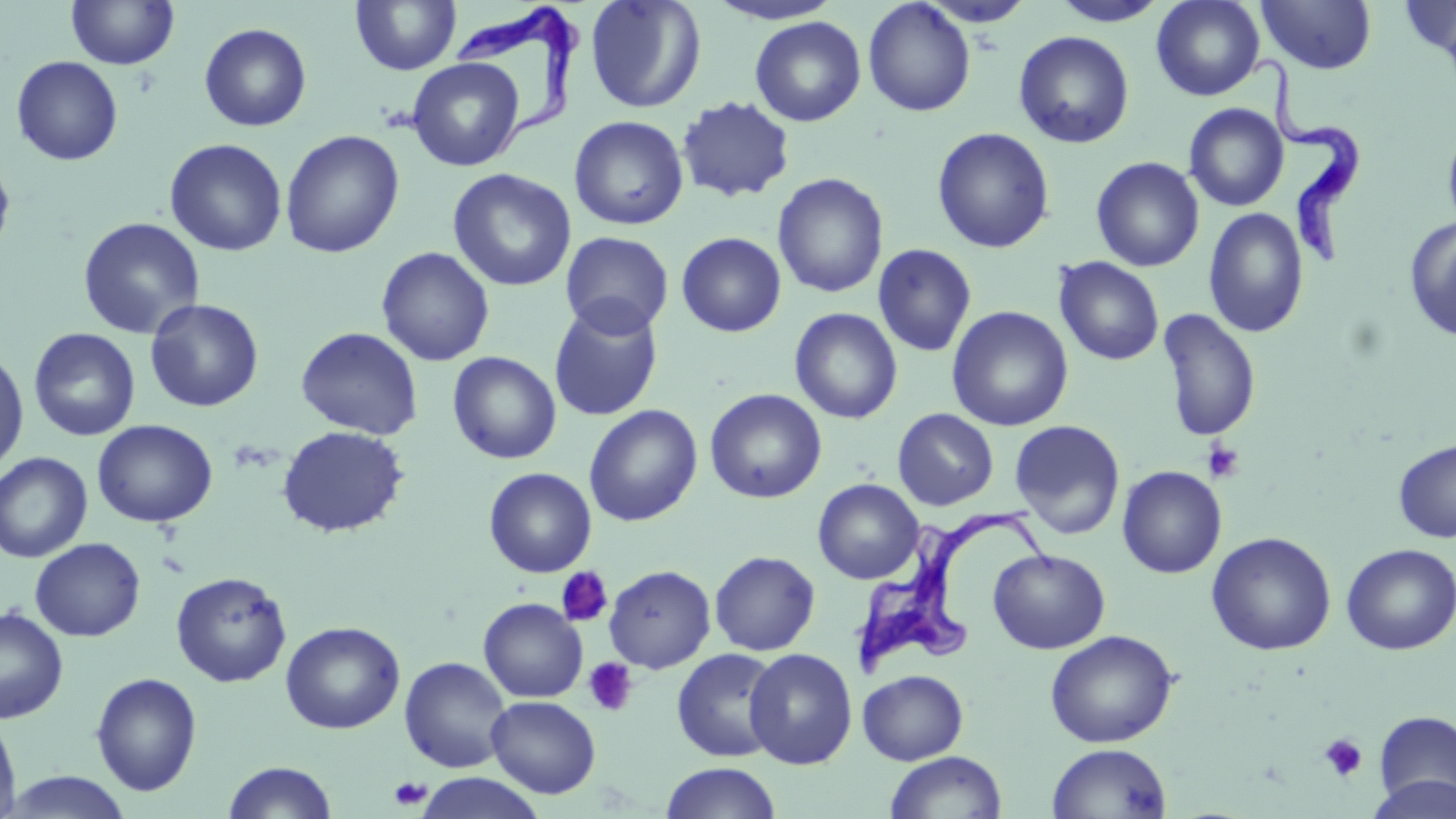 Approximate bounding boxes as (x1,y1)-(x2,y2) corner pairs in pixels. Platelet locations: (1201,439)-(1245,483), (555,568)-(612,627), (584,657)-(638,716), (1319,733)-(1367,782), (388,776)-(432,809). Trypanosoma brucei locations: (451,10)-(586,169), (1253,56)-(1363,274), (851,507)-(1061,685). Uninfected red blood cell locations: (66,0)-(179,69), (350,0)-(462,76), (584,0)-(706,114), (705,0)-(844,26), (1051,0)-(1170,27), (1151,0)-(1265,101), (1256,0)-(1377,75), (1398,0)-(1456,68), (863,1)-(976,117), (919,1)-(1036,27), (750,16)-(866,126), (198,22)-(312,132), (1013,30)-(1134,149), (11,56)-(123,166), (407,57)-(525,172), (676,96)-(795,203), (1184,103)-(1289,211), (569,116)-(689,231), (1442,124)-(1456,236), (933,127)-(1054,253), (280,130)-(404,258), (164,138)-(288,256), (0,155)-(16,262), (1091,156)-(1205,272), (447,169)-(577,293), (772,173)-(888,298), (1204,208)-(1309,338), (77,217)-(205,340), (1404,217)-(1456,343), (560,231)-(673,338), (676,232)-(787,337), (872,244)-(976,357), (376,246)-(495,366), (1053,257)-(1165,366), (145,298)-(264,412), (548,299)-(663,421), (947,305)-(1073,431), (789,307)-(903,424), (1157,309)-(1262,441), (296,326)-(424,440), (28,327)-(141,441), (0,348)-(29,474), (447,351)-(562,465), (704,388)-(827,503), (584,404)-(703,527), (892,408)-(998,510), (92,419)-(218,527), (1009,419)-(1125,540), (276,425)-(410,538), (1393,438)-(1456,542), (0,452)-(93,562), (1117,466)-(1227,578), (484,467)-(596,577), (812,478)-(924,584), (1206,532)-(1337,656), (30,537)-(146,641), (1341,543)-(1456,655), (988,549)-(1110,653), (709,550)-(820,656), (603,564)-(716,673), (171,571)-(292,687), (478,598)-(588,703), (0,606)-(69,723), (280,621)-(405,734), (1045,629)-(1179,747), (672,648)-(783,762), (744,648)-(857,770), (400,657)-(512,773), (858,669)-(968,765), (91,672)-(203,796), (486,696)-(601,798), (1373,709)-(1456,809), (0,716)-(21,819), (1047,743)-(1172,818), (884,751)-(1007,818), (222,760)-(339,818), (660,762)-(782,819), (3,771)-(134,818), (414,772)-(545,818), (1365,774)-(1456,819). Slide-level diagnosis: Trypanosoma brucei. Single field of view. Image is 1456×819 pixels. Captured at 1000x magnification. Thin blood smear. May-Grünwald-Giemsa-stained preparation. Optical microscopy.